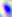

magnification = 400x
modality = micrograph
identification = Toxoplasma gondii